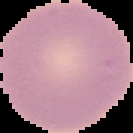

malaria_status: uninfected
image_type: segmented cell region on a black background
image_size: 133×133 pixels
preparation: thin blood film